Locate every malaria parasite.
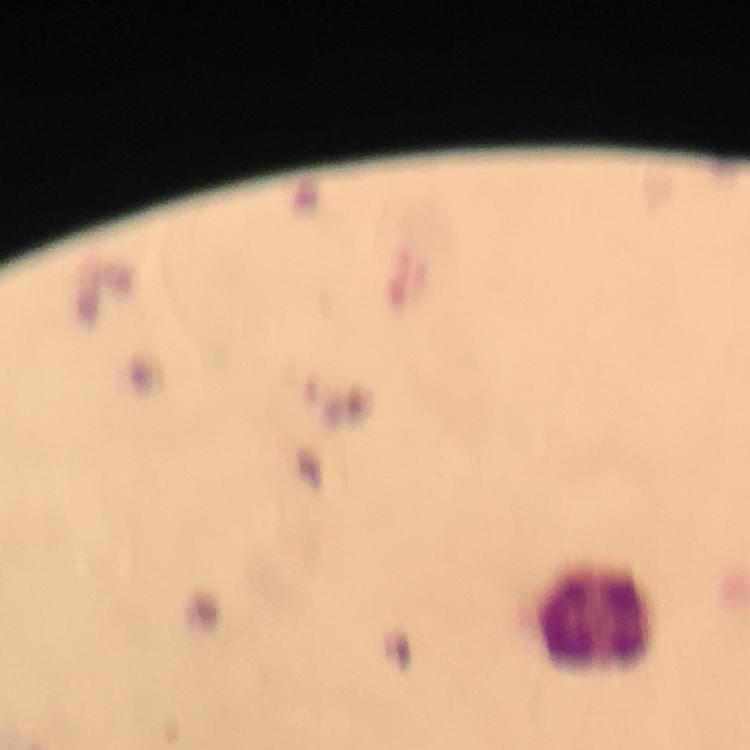

No malaria parasites seen.

image size = 750×750 pixels
capture = smartphone mounted on the microscope
stain = Giemsa
immersion oil = used
leukocyte locations = approximate centers as {x, y} in pixels: {594, 617}
magnification = 100x
cropped from = one field of view
preparation = thick blood film
context = from a malaria diagnostic workup